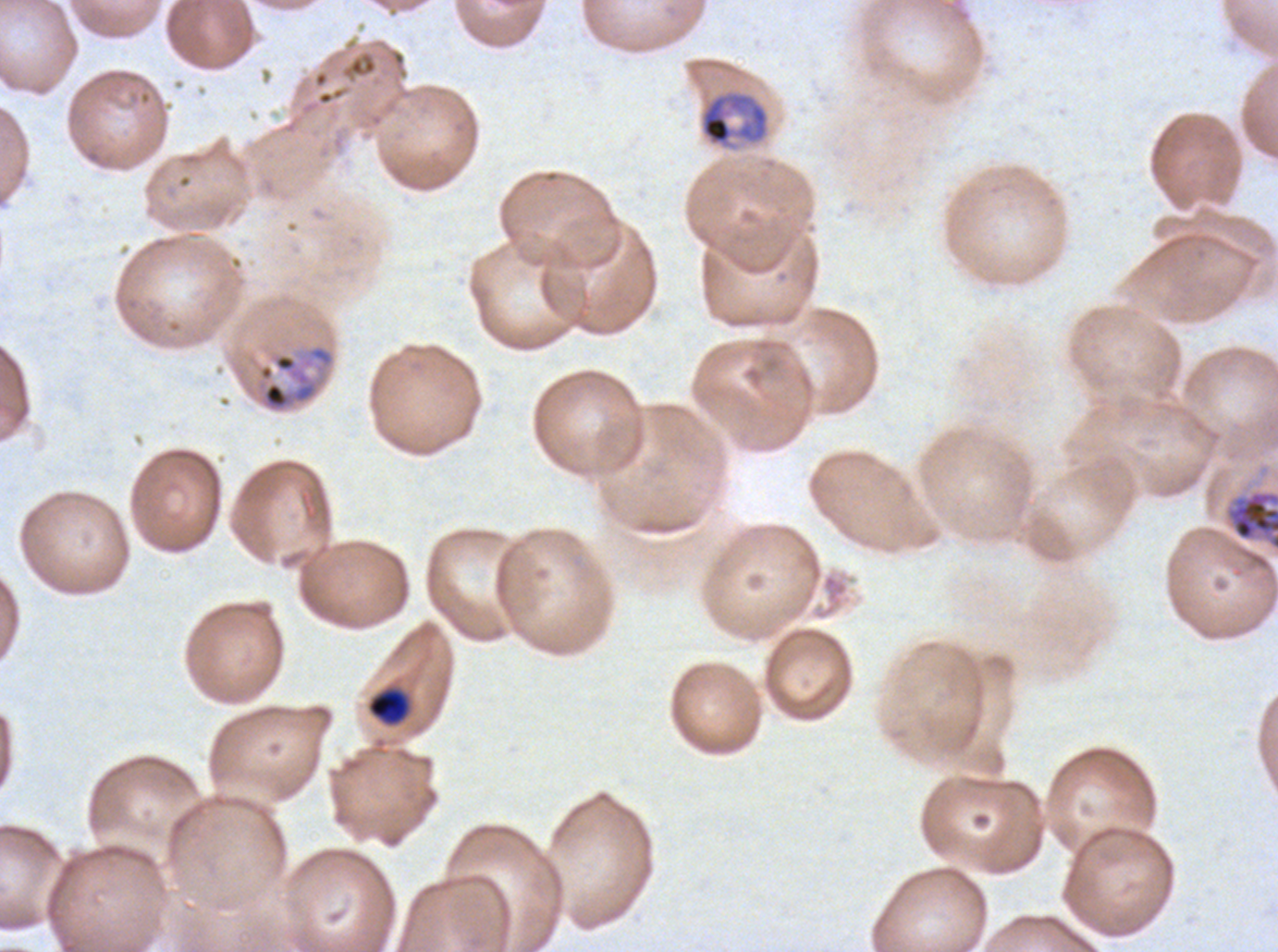

Approximate bounding boxes as [x1, y1, x2, y2] in pixels.
Summary:
  - Late trophozoite locations: [699, 90, 769, 150], [232, 342, 337, 415], [1226, 490, 1277, 551]
  - Late-ring/early-trophozoite locations: [367, 688, 410, 726]
  - Image size: 1278×952 pixels
  - Specimen: ex-vivo P. falciparum culture from a patient in The Gambia, grown for 24 to 48 hours
  - Field of view: sub-image separated from a larger composite
  - Life-cycle stages observed: late-ring/early-trophozoite, late trophozoite
  - Stain: Giemsa
  - Preparation: thin blood smear